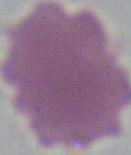
identification: red blood cell
magnification: 1000x
modality: micrograph